Identify the cell.
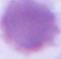
An erythrocyte.

Micrograph. 1000x magnification.